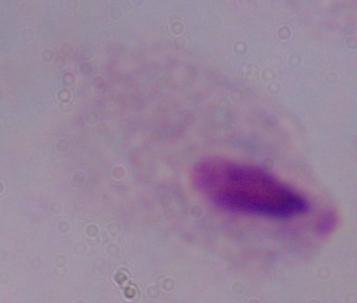
Summary:
  - Modality: micrograph
  - Identification: trichomonad
  - Magnification: 1000x